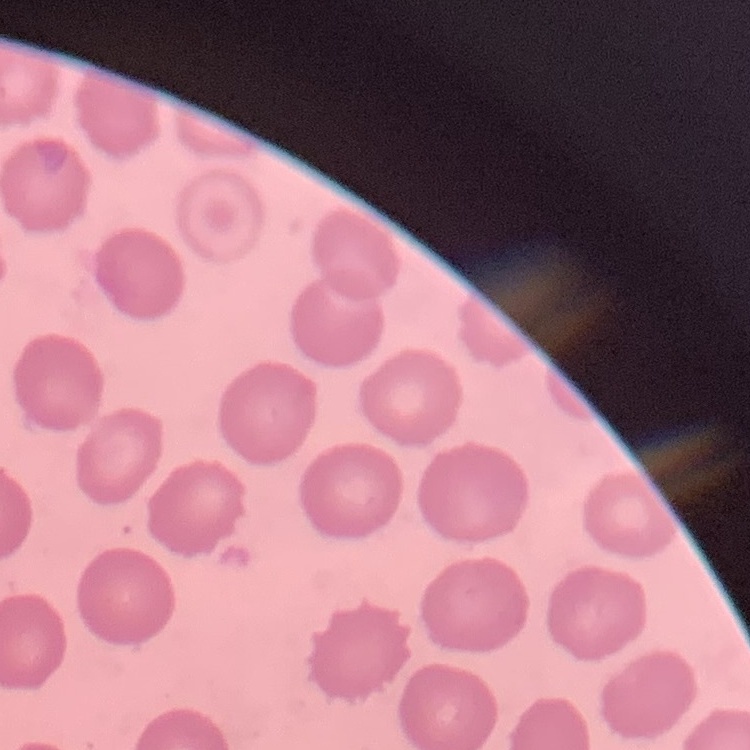
Summary:
  - Erythrocyte morphology: no rouleaux formation
  - Image type: one tile cut from a larger photomicrograph
  - Preparation: thin blood smear
  - Stain: Field's or Giemsa